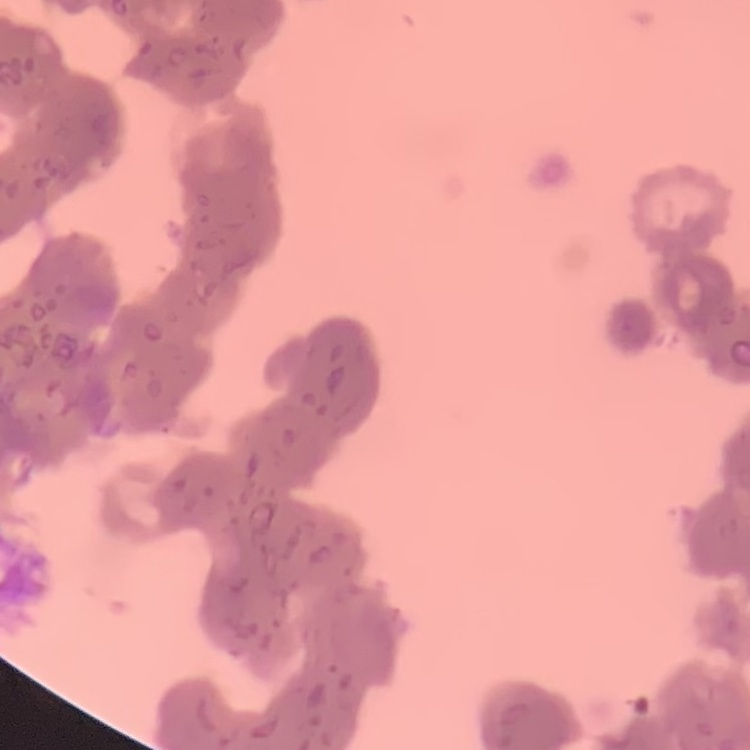

erythrocyte morphology = rouleaux formation
stain = Field's or Giemsa
preparation = thin blood smear
image type = square crop of a larger photomicrograph